Comment on the morphology of the erythrocytes.
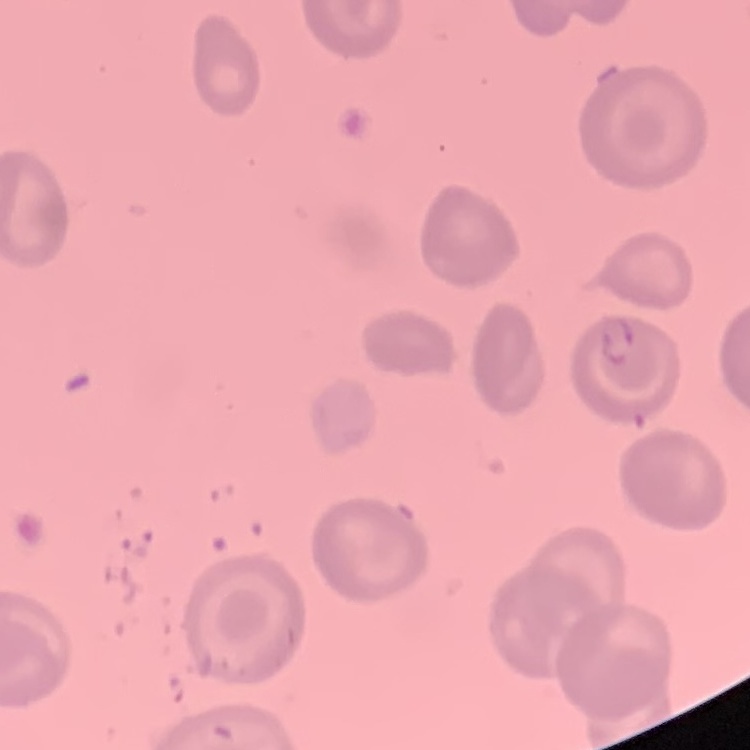
No rouleaux formation.

Summary:
  - Image type: one tile cut from a larger photomicrograph
  - Stain: Field's or Giemsa
  - Preparation: thin blood smear